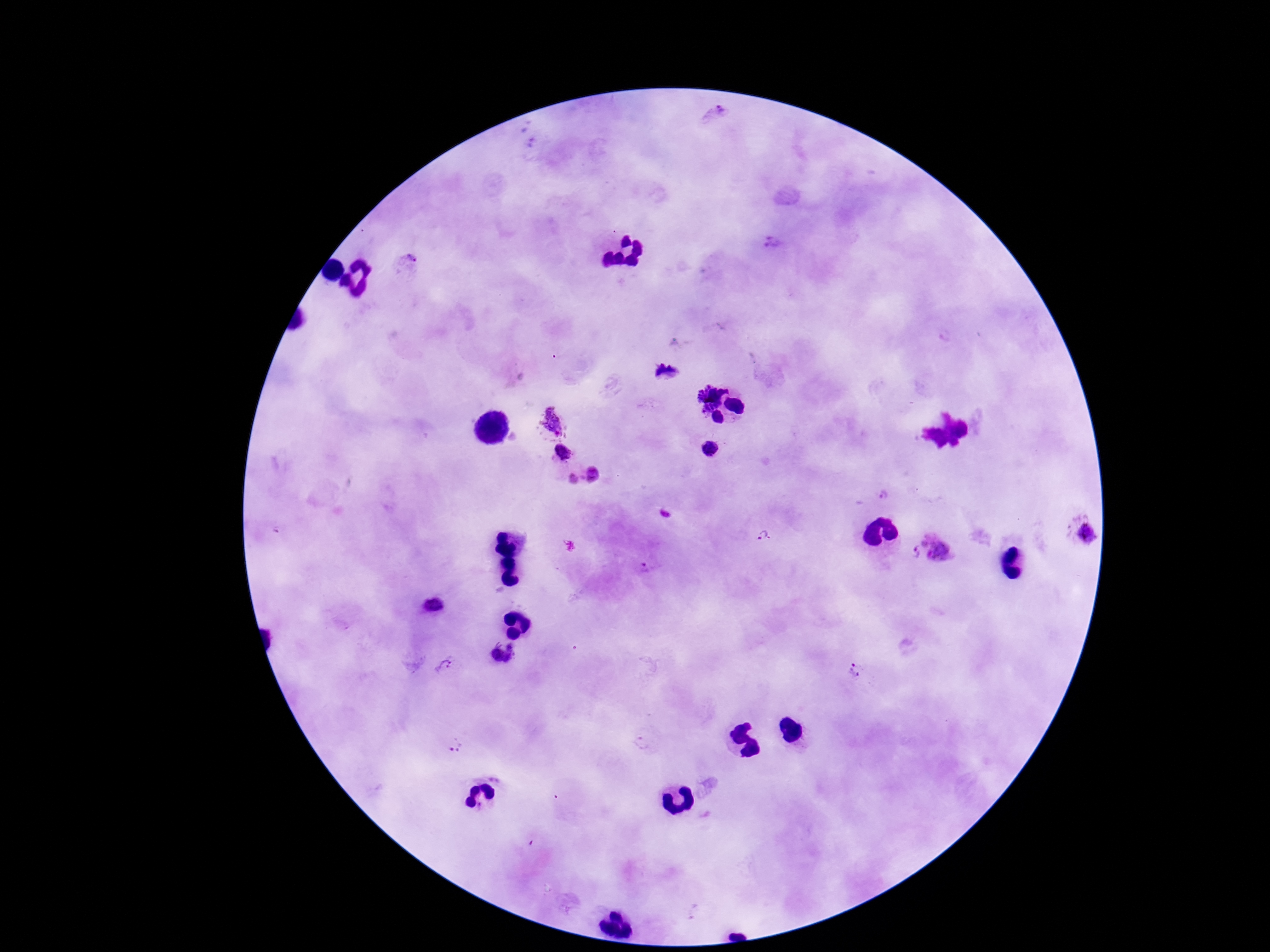

Approximate centers as {x, y} in pixels.
Summary:
  - Plasmodium parasite locations: {721, 109}, {771, 243}, {410, 260}, {665, 371}, {710, 397}, {553, 423}, {563, 453}, {592, 475}, {573, 479}, {883, 497}, {1085, 532}, {762, 535}, {933, 550}, {434, 604}, {503, 653}, {445, 665}, {856, 672}, {454, 745}
  - Image size: 1270×952 pixels
  - Stain: Giemsa
  - Preparation: thick peripheral-blood smear
  - Magnification: 100x
  - Capture: smartphone camera through the microscope eyepiece
  - Patient malaria status: infected
  - Field of view: one from this slide